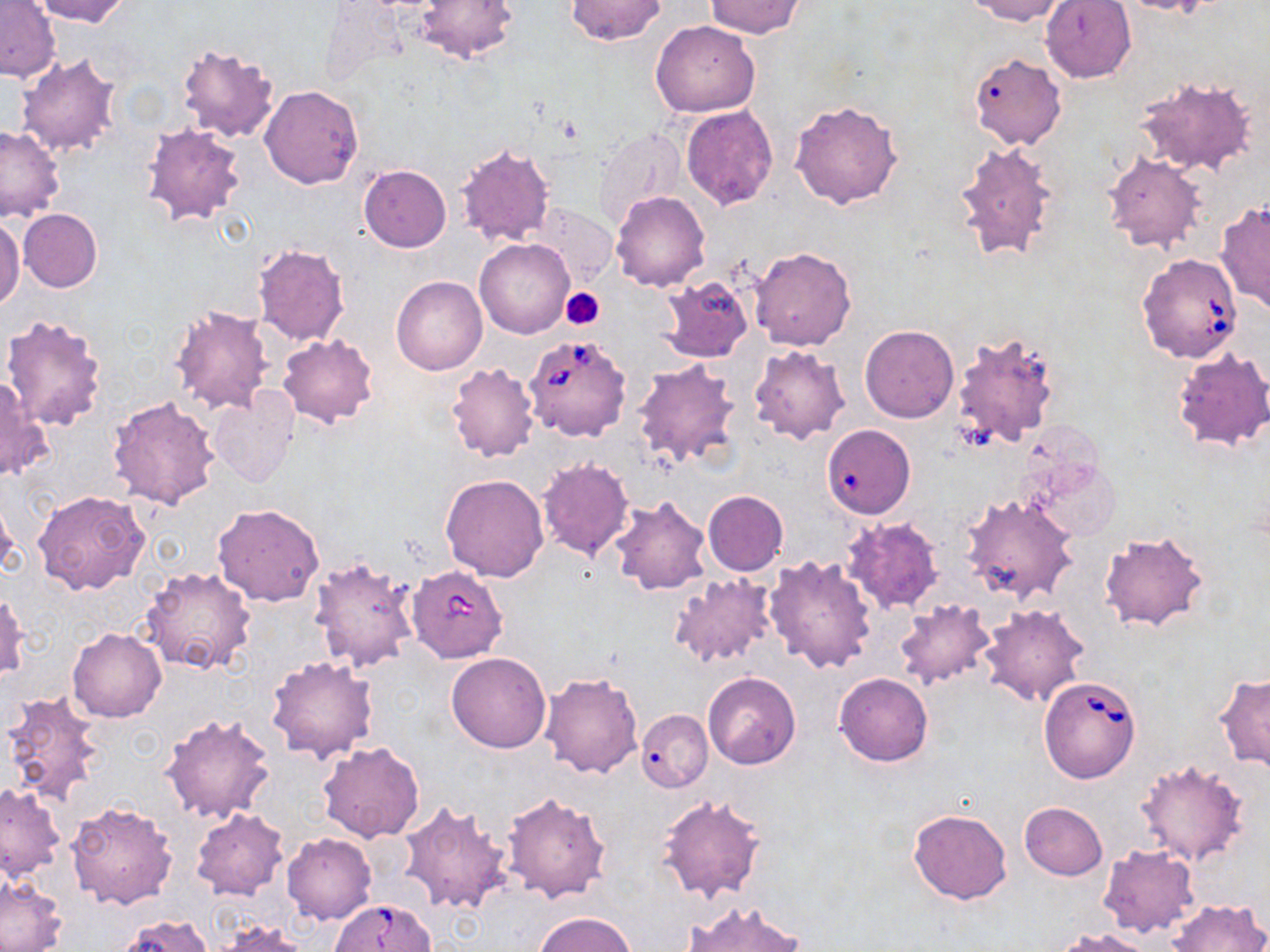

Babesia divergens-infected red blood cell locations = approximate bounding boxes as [x1, y1, x2, y2] in pixels: [1137, 253, 1244, 363], [524, 335, 631, 442], [407, 565, 510, 678], [1039, 676, 1141, 782], [331, 899, 437, 952]
slide-level diagnosis = Babesia divergens
stain = May-Grünwald-Giemsa
modality = optical microscopy
image size = 1270×952 pixels
field of view = single
platelet locations = approximate bounding boxes as [x1, y1, x2, y2] in pixels: [560, 287, 605, 329]
uninfected red blood cell locations = approximate bounding boxes as [x1, y1, x2, y2] in pixels: [32, 0, 130, 26], [413, 0, 519, 65], [563, 0, 668, 46], [966, 0, 1067, 25], [1112, 0, 1218, 16], [0, 1, 60, 82], [705, 1, 803, 37], [1041, 1, 1137, 83], [650, 19, 761, 117], [175, 42, 282, 143], [16, 50, 124, 160], [968, 53, 1066, 150], [1133, 76, 1260, 178], [260, 85, 363, 189], [790, 99, 904, 208], [681, 104, 777, 210], [140, 120, 247, 228], [0, 125, 64, 223], [592, 127, 687, 226], [954, 140, 1059, 260], [453, 143, 555, 250], [1101, 151, 1206, 254], [359, 164, 451, 252], [612, 192, 710, 291], [1217, 200, 1270, 314], [526, 203, 615, 290], [18, 208, 102, 293], [0, 216, 24, 312], [475, 237, 574, 338], [251, 243, 351, 347], [749, 247, 856, 350], [391, 276, 487, 375], [658, 278, 755, 364], [168, 303, 275, 415], [1, 313, 108, 432], [860, 326, 959, 423], [952, 329, 1061, 449], [277, 334, 379, 427], [748, 345, 850, 444], [1172, 346, 1270, 454], [632, 359, 741, 469], [445, 362, 539, 462], [1, 376, 51, 480], [209, 389, 299, 488], [107, 396, 222, 511], [822, 424, 915, 518], [1022, 455, 1119, 543], [536, 457, 635, 560], [441, 473, 550, 581], [32, 490, 149, 597], [702, 491, 789, 577], [960, 493, 1078, 606], [609, 494, 712, 596], [0, 495, 19, 581], [213, 503, 324, 607], [841, 517, 945, 615], [1098, 528, 1209, 634], [308, 555, 420, 672], [764, 555, 878, 673], [141, 565, 257, 678], [671, 574, 776, 668], [1, 591, 29, 683], [895, 599, 995, 688], [979, 603, 1089, 707], [67, 628, 166, 722], [447, 652, 551, 753], [267, 655, 380, 763], [540, 672, 644, 778], [703, 672, 800, 769], [1215, 672, 1270, 771], [835, 673, 933, 765], [2, 691, 108, 806], [636, 709, 712, 792], [159, 713, 275, 825], [319, 742, 424, 841], [1134, 759, 1251, 867], [0, 783, 65, 881], [502, 789, 611, 904], [656, 794, 765, 904], [64, 800, 177, 908], [399, 801, 514, 915], [1019, 801, 1108, 881], [190, 808, 289, 901], [909, 808, 1013, 904], [282, 832, 376, 924], [1098, 845, 1201, 938], [0, 874, 66, 951], [1165, 898, 1268, 952], [685, 901, 808, 952], [532, 912, 637, 952], [112, 915, 218, 952], [208, 918, 316, 951], [1055, 927, 1158, 952]
preparation = thin blood smear
magnification = 1000x